Assess the morphology of the erythrocytes.
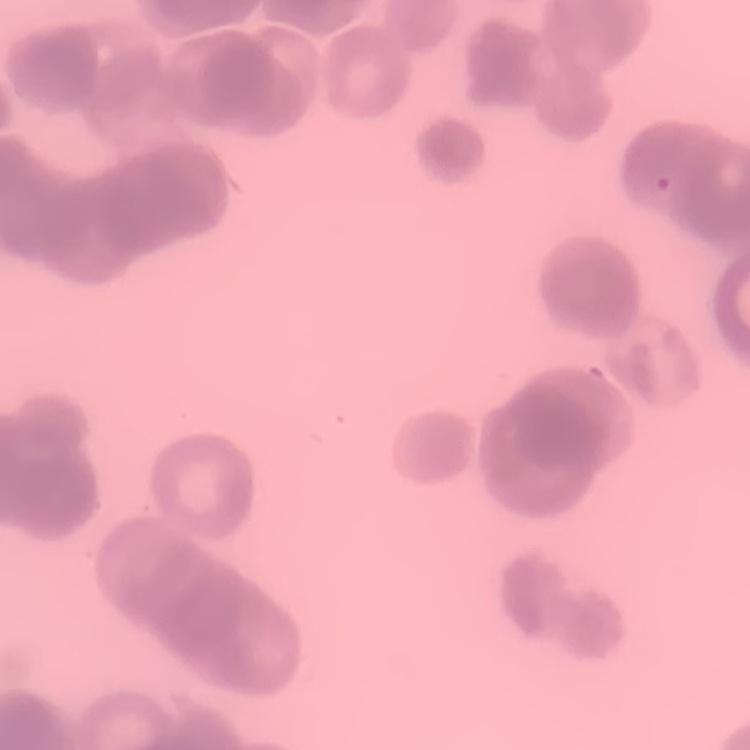

They show rouleaux formation.

Summary:
  - Stain: Field's or Giemsa
  - Image type: one tile cut from a larger photomicrograph
  - Preparation: thin blood smear